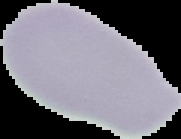

Summary:
  - Result: negative for Plasmodium parasites
  - Image type: cell region segmented out of the field of view; surrounding area masked to black
  - Preparation: thin blood film
  - Image size: 181×139 pixels